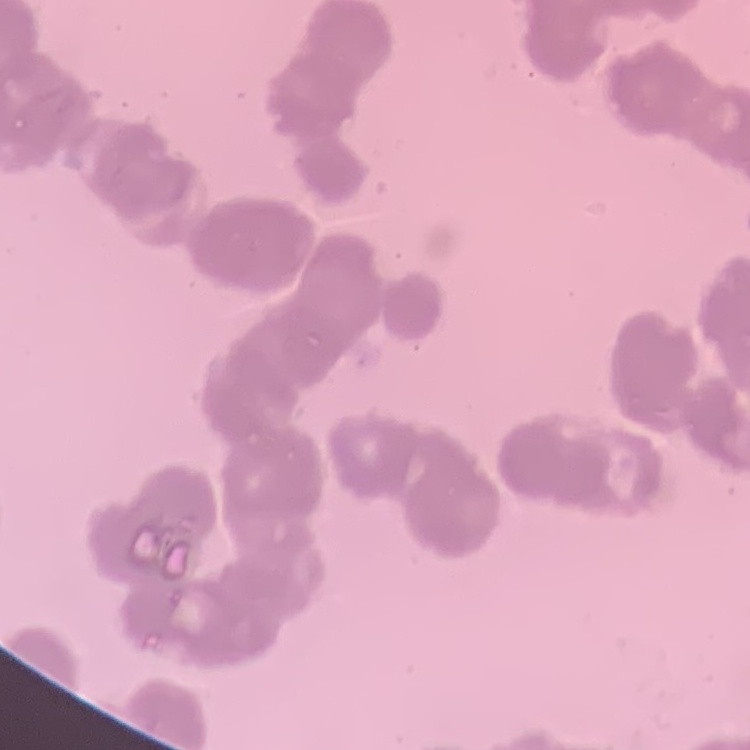
red blood cell morphology = rouleaux formation
preparation = thin peripheral smear
image type = one tile cut from a larger photomicrograph
stain = Field's or Giemsa